Locate and identify every blood parasite.
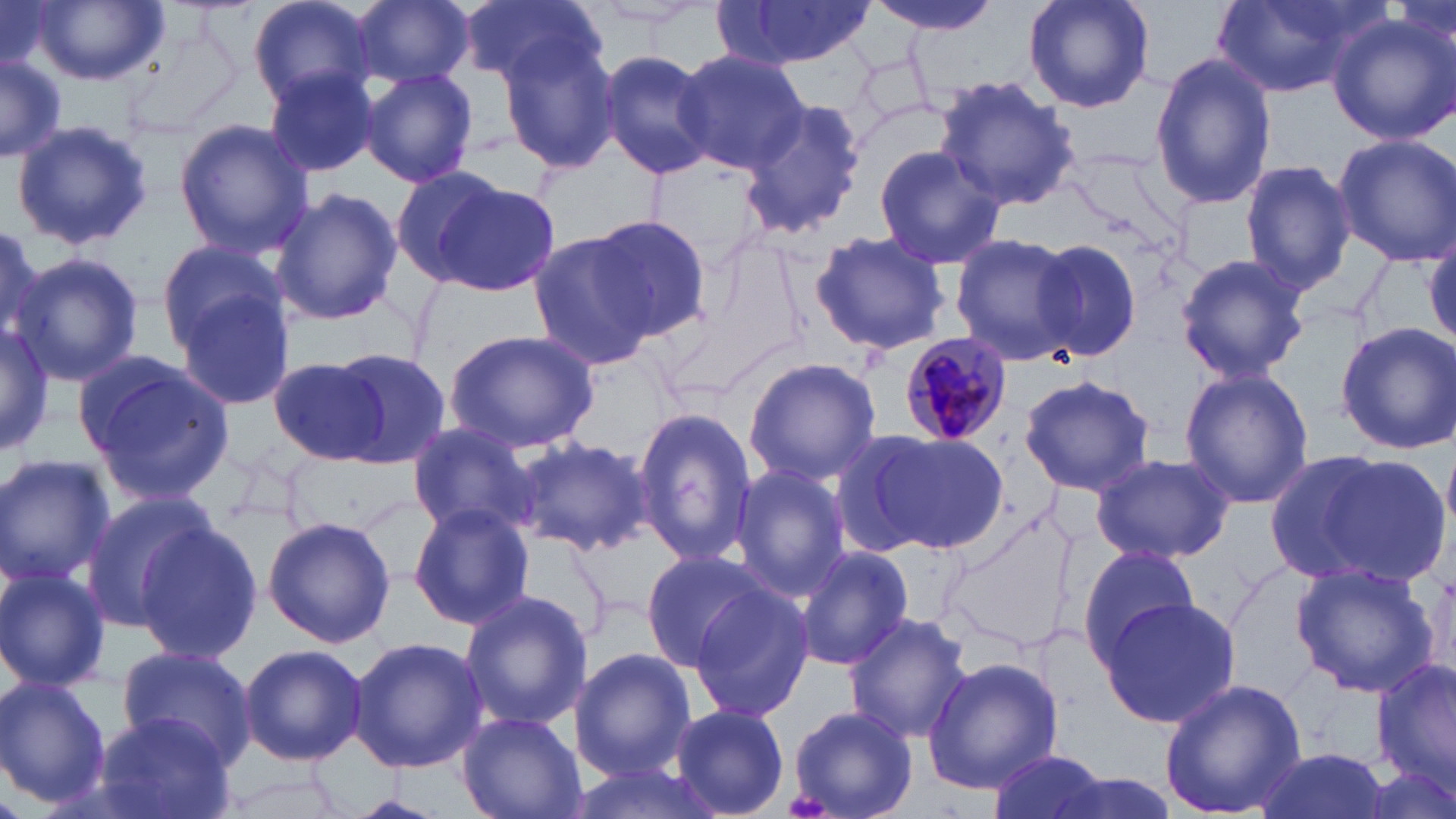
Approximate bounding boxes as (x1,y1)-(x2,y2) corner pairs in pixels.
Plasmodium malariae-infected red blood cells: (897,330)-(1013,446).
No Plasmodium falciparum, Plasmodium ovale, Plasmodium vivax, Babesia divergens, or Trypanosoma brucei observed.

slide-level diagnosis = Plasmodium malariae
magnification = 1000x
modality = optical microscopy
image size = 1456×819 pixels
field of view = single
preparation = thin blood smear
stain = May-Grünwald-Giemsa
uninfected red blood cell locations = approximate bounding boxes as (x1,y1)-(x2,y2) corner pairs in pixels: (249,0)-(380,110), (353,0)-(473,87), (869,0)-(997,38), (1022,0)-(1154,115), (1213,0)-(1380,97), (0,1)-(54,69), (461,1)-(606,91), (709,1)-(880,70), (28,2)-(166,87), (578,2)-(717,30), (1328,14)-(1456,145), (497,26)-(622,174), (596,49)-(717,178), (674,50)-(810,173), (0,52)-(67,162), (1149,53)-(1276,208), (359,66)-(480,189), (264,67)-(380,177), (935,75)-(1082,213), (740,98)-(867,238), (8,120)-(153,251), (174,120)-(312,257), (1332,134)-(1456,266), (872,143)-(1005,270), (1239,160)-(1357,298), (389,167)-(508,284), (426,178)-(563,293), (270,189)-(404,325), (583,217)-(712,342), (0,223)-(62,360), (808,230)-(952,354), (525,231)-(659,373), (947,232)-(1078,363), (155,237)-(287,351), (1031,239)-(1141,360), (11,252)-(144,387), (1173,253)-(1311,383), (173,284)-(297,413), (0,318)-(54,458), (1334,321)-(1456,456), (443,330)-(598,452), (321,348)-(450,466), (76,355)-(233,504), (742,357)-(882,485), (270,358)-(395,463), (1177,367)-(1315,509), (1019,373)-(1155,496), (631,404)-(757,572), (404,423)-(536,540), (864,430)-(1007,552), (510,437)-(649,553), (1268,447)-(1450,590), (1090,451)-(1236,565), (0,454)-(114,590), (729,465)-(851,599), (79,493)-(224,632), (407,501)-(534,630), (263,516)-(396,649), (134,522)-(262,664), (1077,543)-(1202,667), (796,546)-(914,671), (639,549)-(770,671), (1288,562)-(1440,698), (0,566)-(111,693), (686,583)-(814,723), (458,589)-(591,732), (1095,597)-(1242,728), (842,613)-(973,744), (350,636)-(488,772), (238,643)-(367,765), (115,646)-(259,769), (573,649)-(695,780), (1374,656)-(1456,794), (923,657)-(1062,794), (1158,677)-(1306,818), (0,678)-(111,808), (670,703)-(791,818), (786,705)-(918,819), (94,710)-(235,819), (457,710)-(585,819), (986,748)-(1111,819), (1249,748)-(1394,819), (570,758)-(722,819), (211,762)-(356,819), (341,792)-(448,818)